Classify this cell by malaria status.
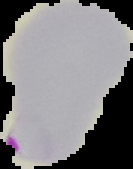
Parasitized.

preparation = thin blood smear
image type = segmented cell region with the area outside set to black
image size = 133×169 pixels